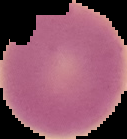
Summary:
  - Preparation: thin blood film
  - Result: no malaria parasites detected
  - Image size: 127×139 pixels
  - Image type: segmented cell region on a black background